Identify the cell.
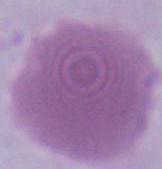
An erythrocyte.

modality = micrograph
magnification = 1000x